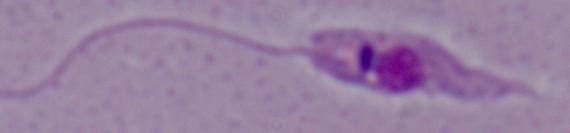
modality = photomicrograph
magnification = 1000x
identification = Leishmania